Evaluate for malaria.
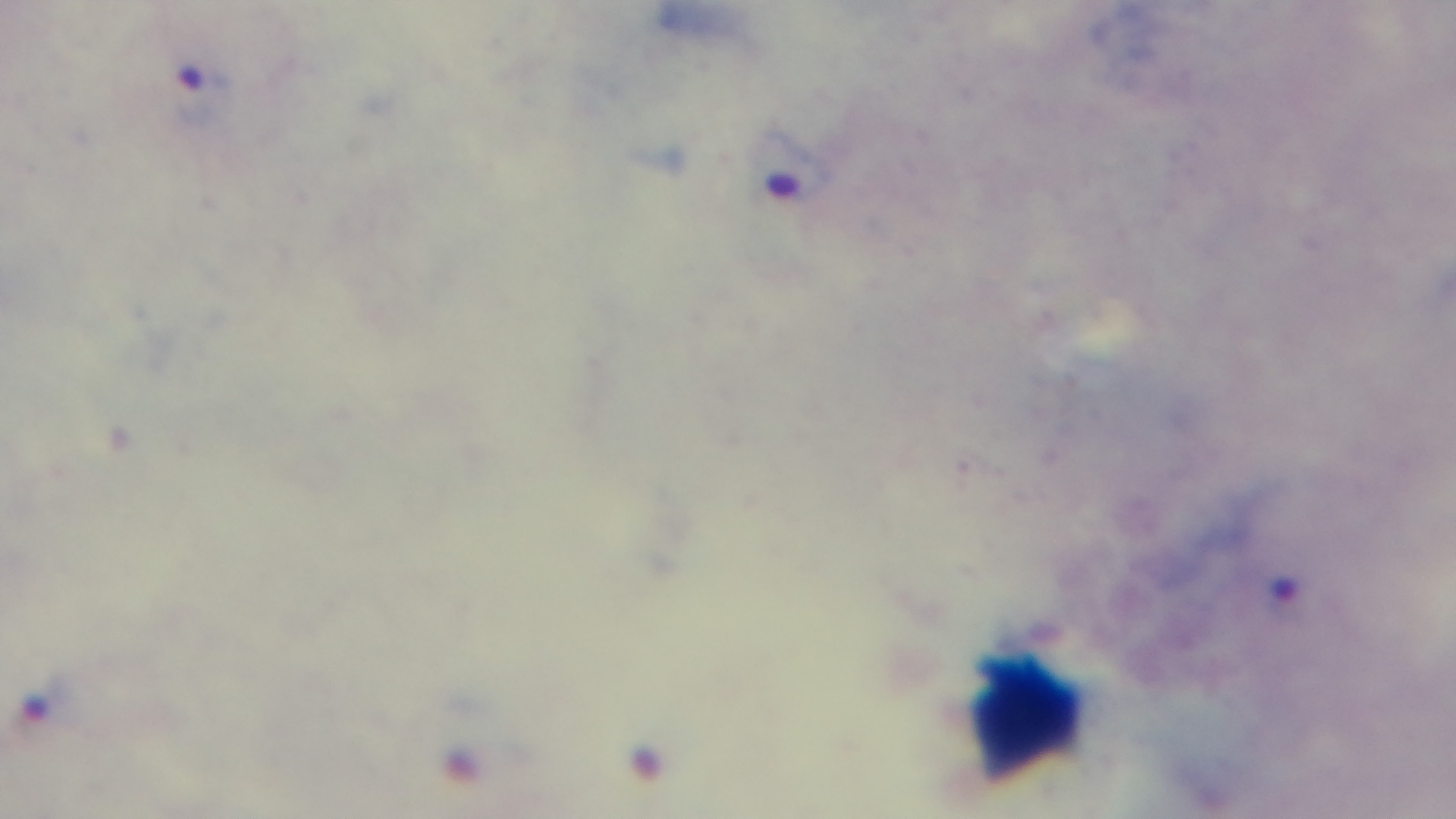
Infected.

{
  "modality": "light microscopy",
  "objective": "100x oil immersion",
  "stain": "Giemsa",
  "field_of_view": "single",
  "capture": "mounted 4K digital camera",
  "preparation": "thick"
}